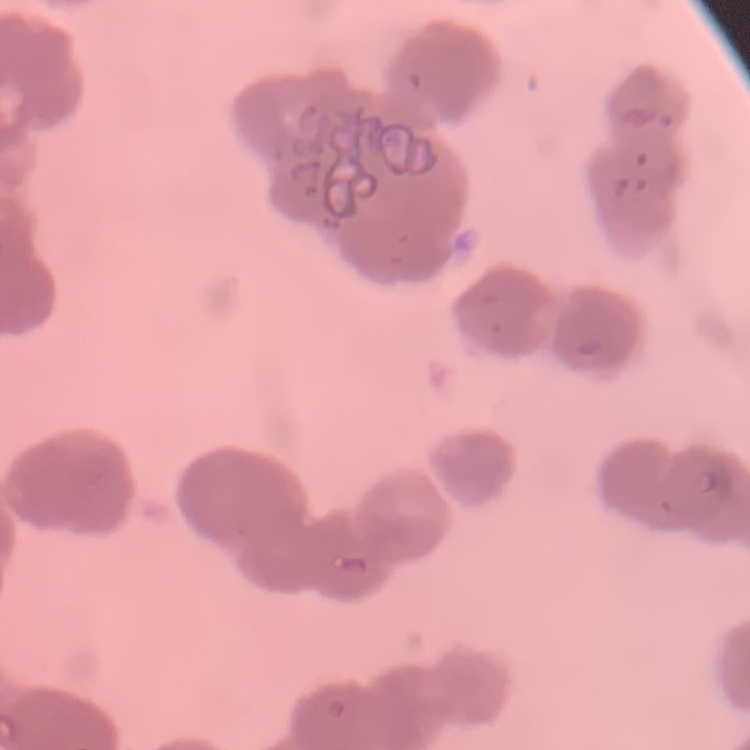

The erythrocytes show rouleaux formation. Square crop of a larger photomicrograph. Thin peripheral smear. Stained with either Field's or Giemsa.